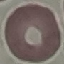

Summary:
  - Malaria status: uninfected
  - Capture: smartphone through the microscope eyepiece
  - Image type: cell patch, automatically extracted from a larger field of view and resized to 64 × 64 pixels
  - Preparation: thin blood film
  - Stain: Giemsa